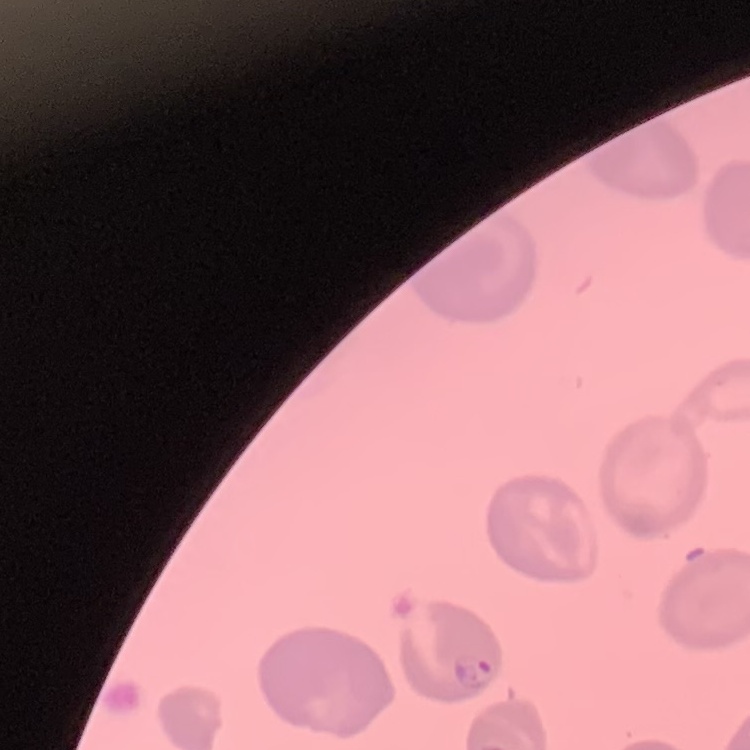
The red blood cells exhibit no rouleaux formation. Thin blood film. One tile cut from a larger photomicrograph. Field's or Giemsa stain.